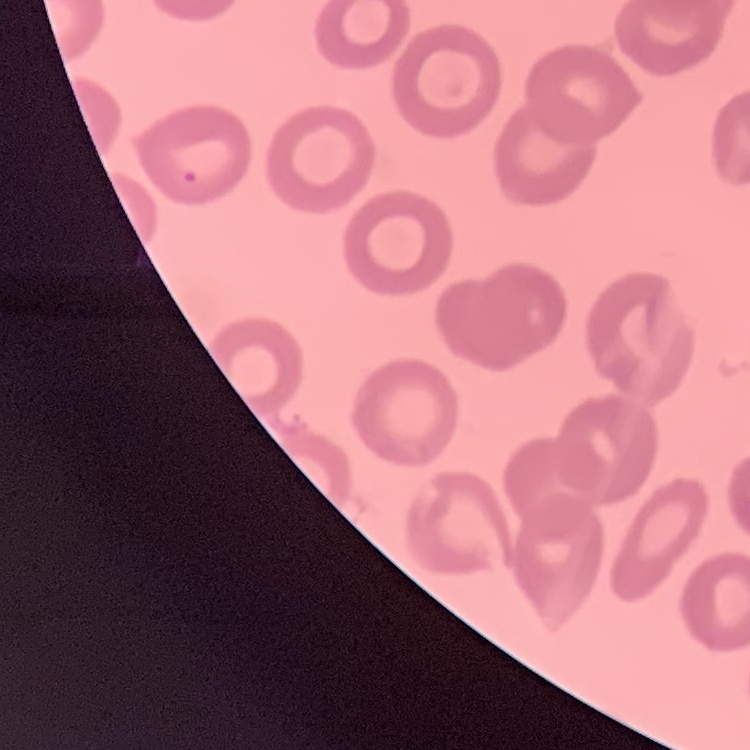 The erythrocytes exhibit no rouleaux formation. One tile cut from a larger photomicrograph. Stained with either Field's or Giemsa. Thin blood film.